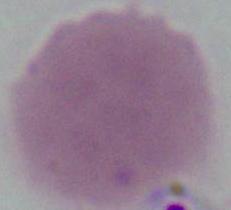

Summary:
  - Modality: photomicrograph
  - Identification: erythrocyte
  - Magnification: 1000x